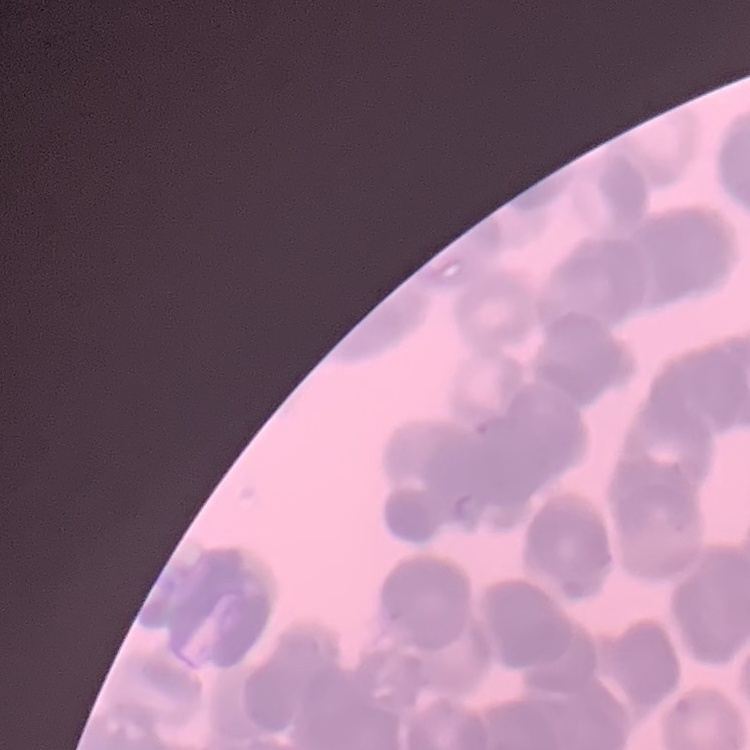 The erythrocytes show rouleaux formation. Stained with either Field's or Giemsa. Thin blood smear. Square crop of a larger photomicrograph.